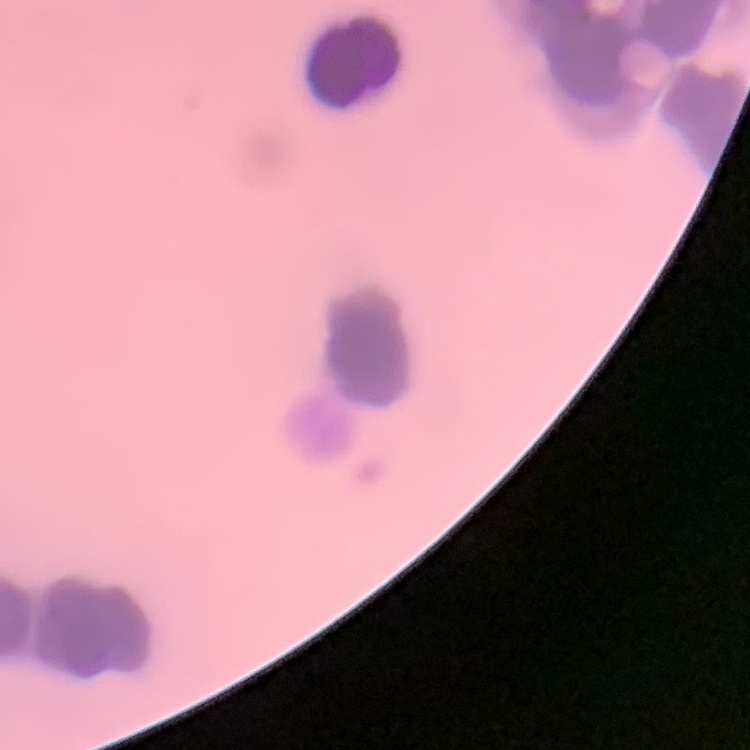

erythrocyte morphology = rouleaux formation
image type = square crop of a larger photomicrograph
stain = Field's or Giemsa
preparation = thin peripheral smear